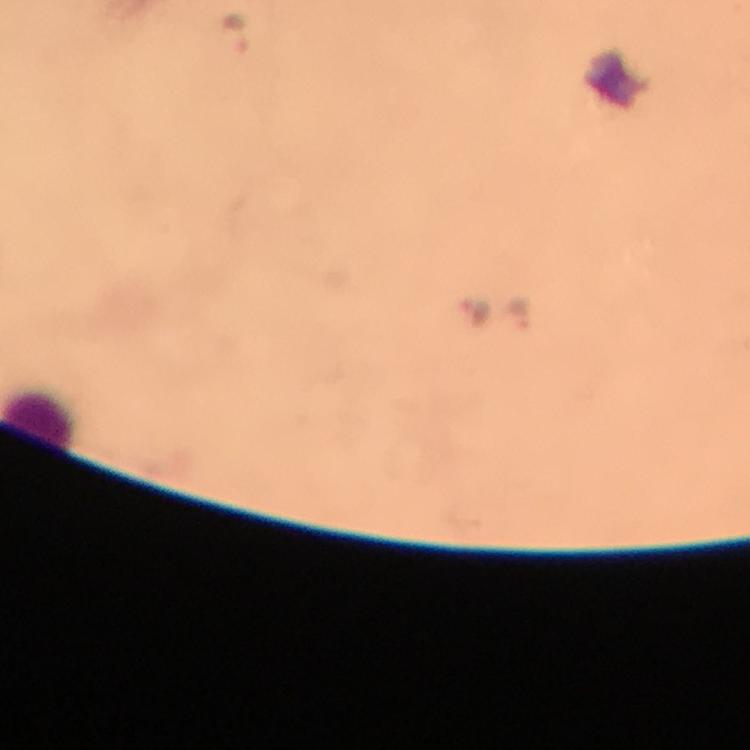
capture = smartphone photograph through a microscope
immersion oil = applied
preparation = thick blood film
stain = Giemsa
context = from a diagnostic examination for malaria
leukocyte locations = approximate object centers, in pixels from the top-left corner: (x=42, y=424)
magnification = 100x
image size = 750×750 pixels
Plasmodium parasite locations = approximate object centers, in pixels from the top-left corner: (x=235, y=31), (x=479, y=311), (x=521, y=314)
cropped from = a single field of view